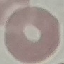
Summary:
  - Malaria status: uninfected
  - Capture: smartphone through the microscope eyepiece
  - Preparation: thin blood smear
  - Image type: automatically extracted cell patch, resized to 64 × 64 pixels
  - Stain: Giemsa